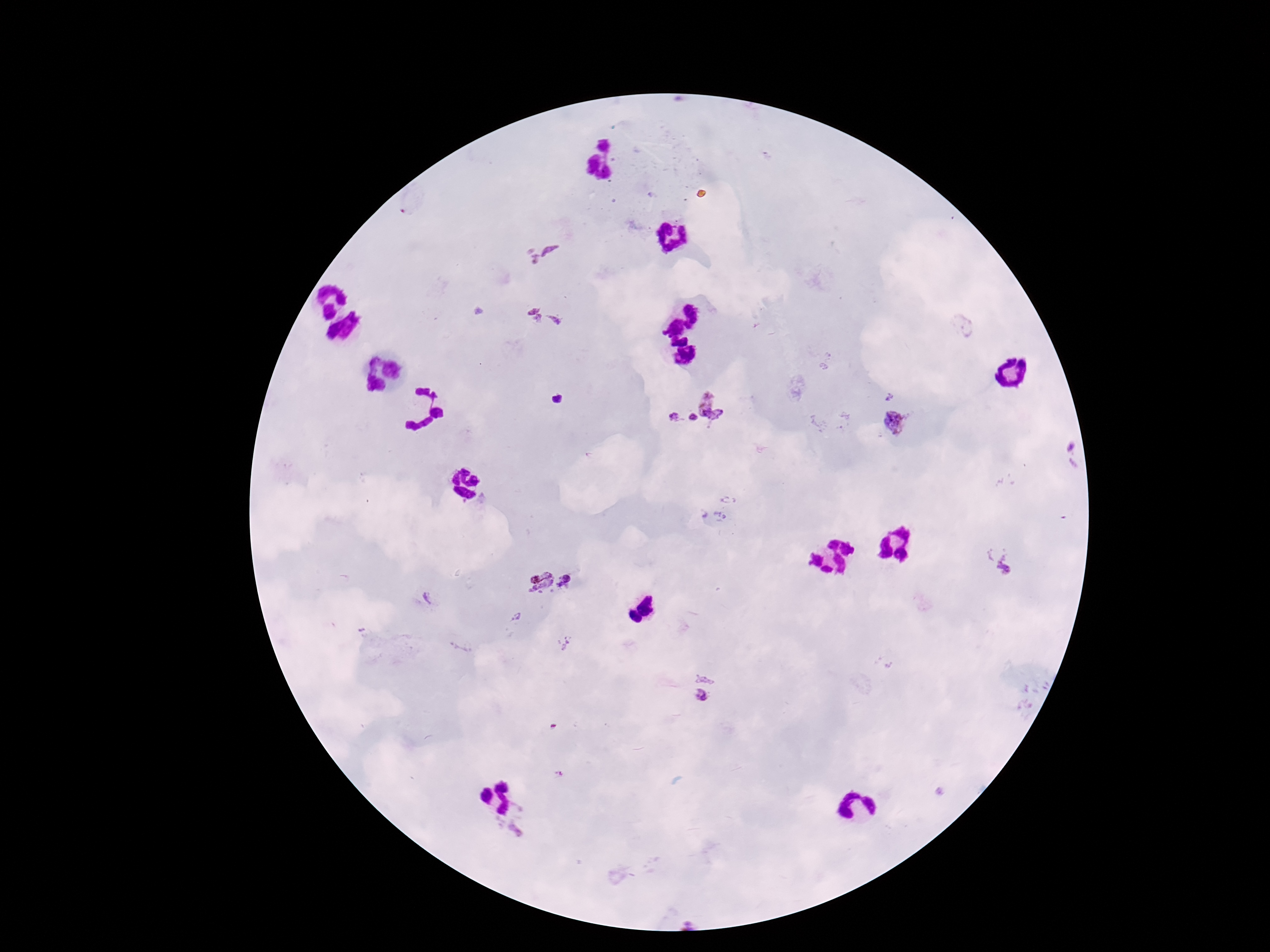
Approximate centers as [x, y] in pixels.
Summary:
  - Plasmodium parasite locations: [542, 253], [547, 319], [717, 405], [693, 418], [674, 419], [894, 424], [1072, 456], [1000, 562], [571, 580], [539, 581], [518, 618], [707, 676], [702, 698], [525, 824]
  - Capture: smartphone camera through the microscope eyepiece
  - Magnification: 100x
  - Stain: Giemsa
  - Field of view: single
  - Image size: 1270×952 pixels
  - Preparation: thick blood smear
  - Patient malaria status: positive